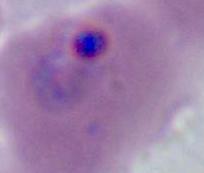

identification = Plasmodium
magnification = 400x or 1000x
modality = micrograph